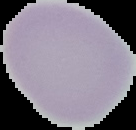
The area outside the segmented cell region is set to black. Image is 136×130 pixels. From a thin blood smear. Result: no Plasmodium parasites detected.